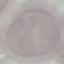

Summary:
  - Malaria status: uninfected
  - Capture: smartphone through the microscope eyepiece
  - Stain: Giemsa
  - Preparation: thin blood film
  - Image type: cell patch, automatically extracted from a larger field of view and resized to 64 × 64 pixels